Report the malaria status of this cell.
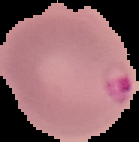

Parasitized.

preparation = thin blood smear
image size = 139×142 pixels
image type = segmented cell region on a black background